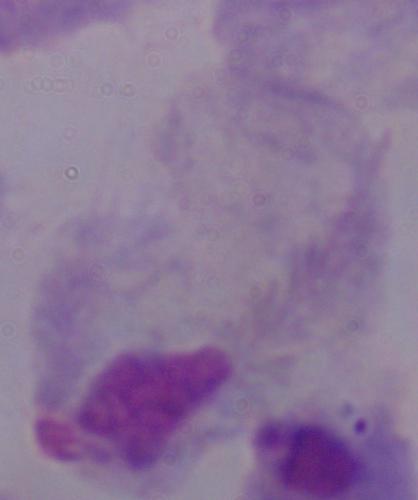

modality = micrograph
magnification = 1000x
identification = trichomonad